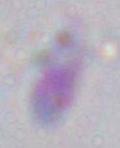

Captured at 1000x magnification. Toxoplasma gondii is seen. Photomicrograph.